Report the malaria status of this cell.
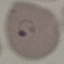
It is parasitized.

{
  "capture": "smartphone through the microscope eyepiece",
  "stain": "Giemsa",
  "preparation": "thin blood smear",
  "image_type": "automatically extracted cell patch, resized to 64 × 64 pixels"
}